Name the parasite shown.
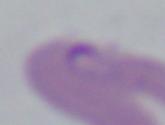

This is Babesia.

Summary:
  - Magnification: 1000x
  - Modality: micrograph